Classify this cell by malaria status.
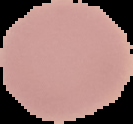
It is uninfected.

{
  "image_size": "133×124 pixels",
  "image_type": "cell region segmented out of the field of view; surrounding area masked to black",
  "preparation": "thin blood film"
}